Assess this cell for malaria.
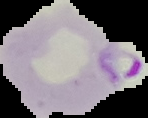

Parasitized.

From a thin blood smear. Cell region segmented out of the field of view; the surrounding area is masked to black. Image is 148×118 pixels.